Classify this cell by malaria status.
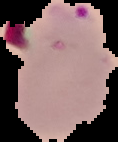
It is parasitized.

{
  "preparation": "thin blood film",
  "image_size": "118×142 pixels",
  "image_type": "segmented cell region on a black background"
}